Locate every blood parasite and identify its species.
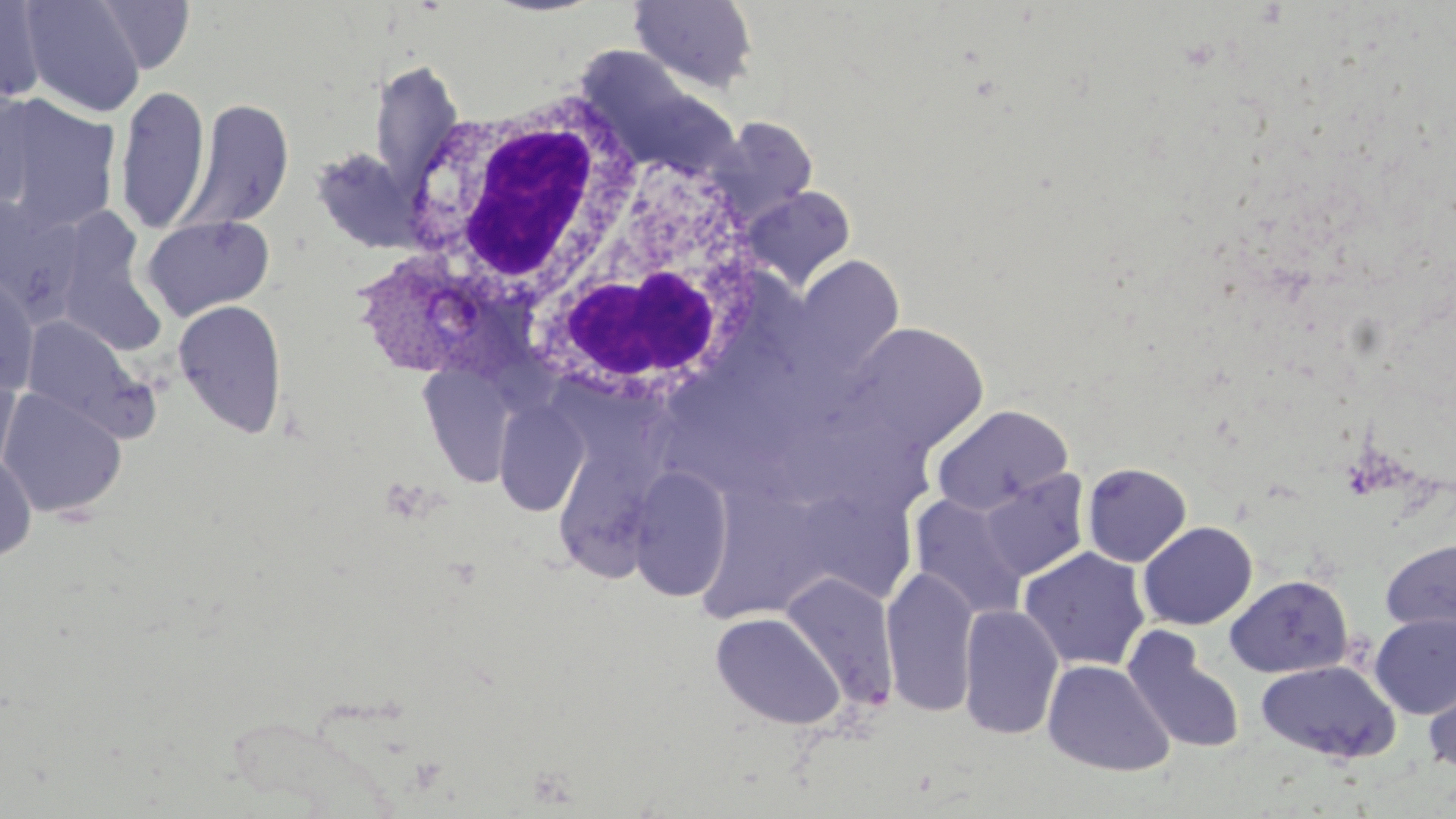
Approximate bounding boxes as [x1, y1, x2, y2] in pixels.
Plasmodium vivax-infected red blood cells: [357, 259, 517, 385].
No Plasmodium falciparum, Plasmodium ovale, Plasmodium malariae, Babesia divergens, or Trypanosoma brucei observed.

Summary:
  - Uninfected red blood cell locations: [20, 0, 146, 117], [94, 0, 195, 74], [630, 0, 760, 94], [0, 1, 48, 103], [575, 45, 738, 180], [369, 59, 465, 193], [0, 85, 39, 211], [114, 85, 210, 234], [1, 96, 122, 233], [182, 99, 294, 232], [715, 117, 819, 220], [309, 146, 427, 254], [740, 186, 856, 292], [0, 196, 87, 317], [62, 206, 170, 355], [141, 213, 276, 322], [791, 255, 905, 380], [0, 276, 39, 395], [172, 300, 288, 437], [20, 315, 150, 438], [842, 323, 989, 458], [418, 365, 517, 486], [0, 369, 20, 479], [0, 388, 127, 519], [494, 399, 590, 515], [556, 401, 673, 599], [930, 404, 1073, 516], [0, 452, 37, 563], [1082, 462, 1192, 567], [626, 464, 735, 604], [977, 470, 1091, 582], [684, 485, 833, 644], [909, 493, 1030, 619], [808, 497, 917, 607], [1138, 521, 1258, 630], [1380, 538, 1456, 636], [1018, 547, 1150, 673], [881, 566, 980, 718], [782, 572, 900, 709], [1225, 574, 1353, 678], [959, 603, 1065, 741], [710, 611, 846, 729], [1369, 612, 1456, 719], [1123, 628, 1247, 754], [1042, 659, 1175, 777], [1256, 660, 1400, 763], [1422, 664, 1456, 776]
  - White blood cell locations: [407, 88, 666, 351], [502, 134, 773, 418]
  - Slide-level diagnosis: Plasmodium vivax
  - Stain: May-Grünwald-Giemsa
  - Magnification: 1000x
  - Preparation: thin blood smear
  - Image size: 1456×819 pixels
  - Modality: optical microscopy
  - Field of view: one of a larger specimen